Identify the cell.
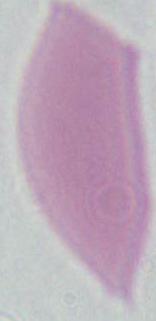
This is an erythrocyte.

magnification: 1000x
modality: micrograph